Locate every Plasmodium parasite.
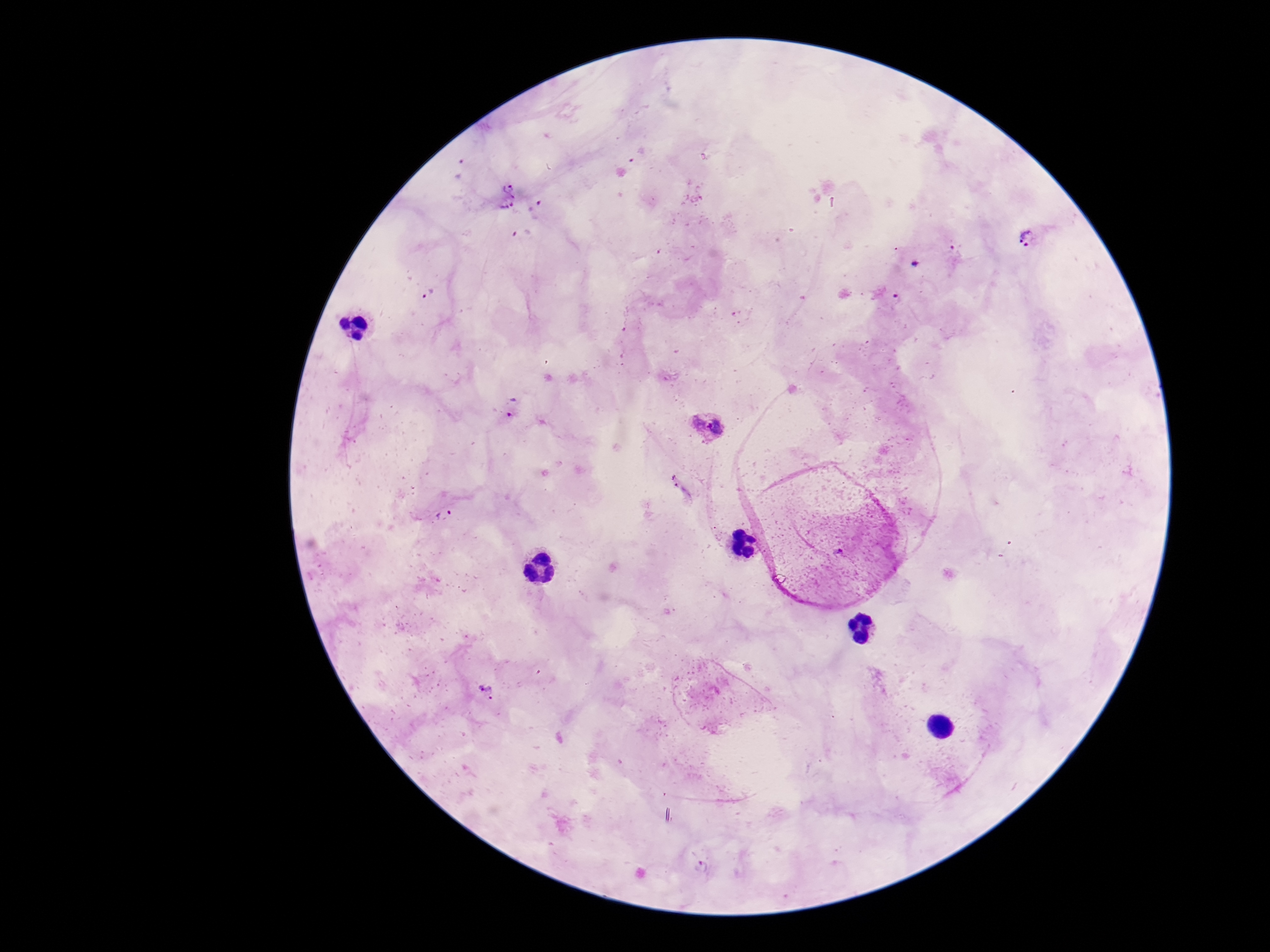
Approximate centers as (x, y) in pixels.
Plasmodium parasites: (508, 184), (507, 203), (537, 207), (1030, 239), (430, 293), (897, 298), (512, 407), (710, 426), (444, 513), (487, 690), (702, 866).

{
  "patient_malaria_status": "positive",
  "preparation": "thick blood film",
  "stain": "Giemsa",
  "capture": "smartphone camera through the microscope eyepiece",
  "image_size": "1270×952 pixels",
  "magnification": "100x",
  "field_of_view": "single"
}